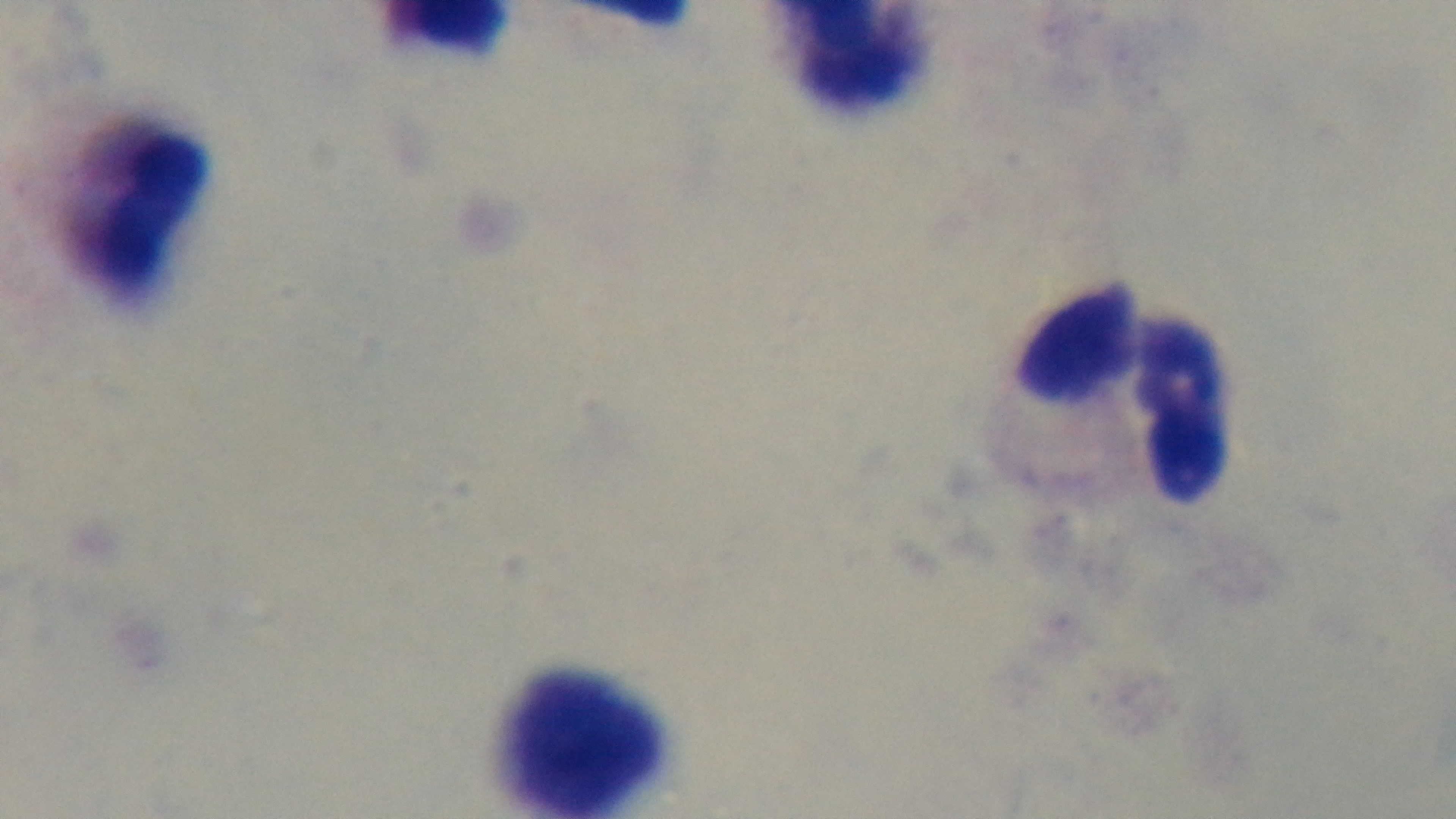

Summary:
  - Objective: 100x oil immersion
  - Preparation: thick
  - Malaria status: uninfected
  - Field of view: single
  - Modality: light microscopy
  - Capture: mounted 4K digital camera
  - Stain: Giemsa